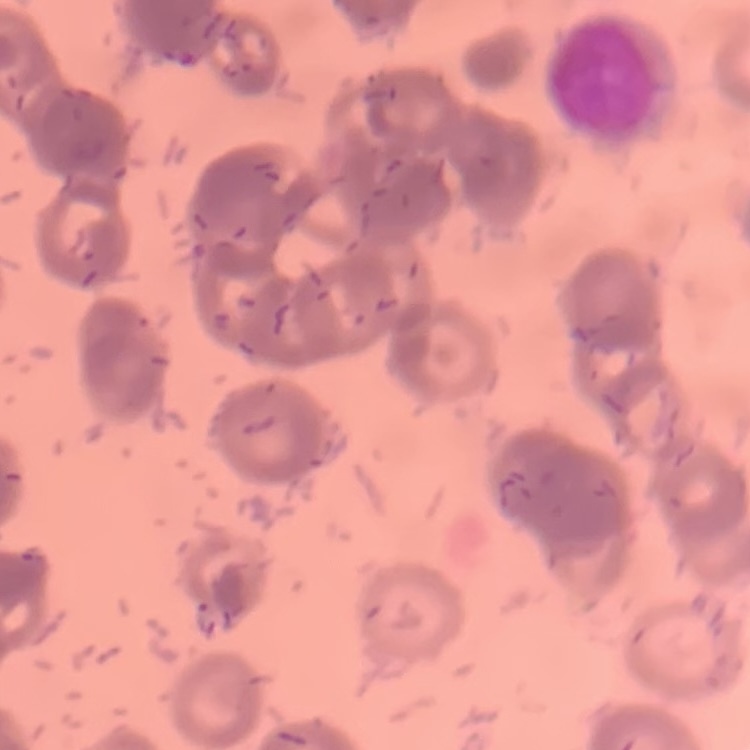

The red blood cells exhibit rouleaux formation. Field's or Giemsa stain. Thin blood film. One tile cut from a larger photomicrograph.